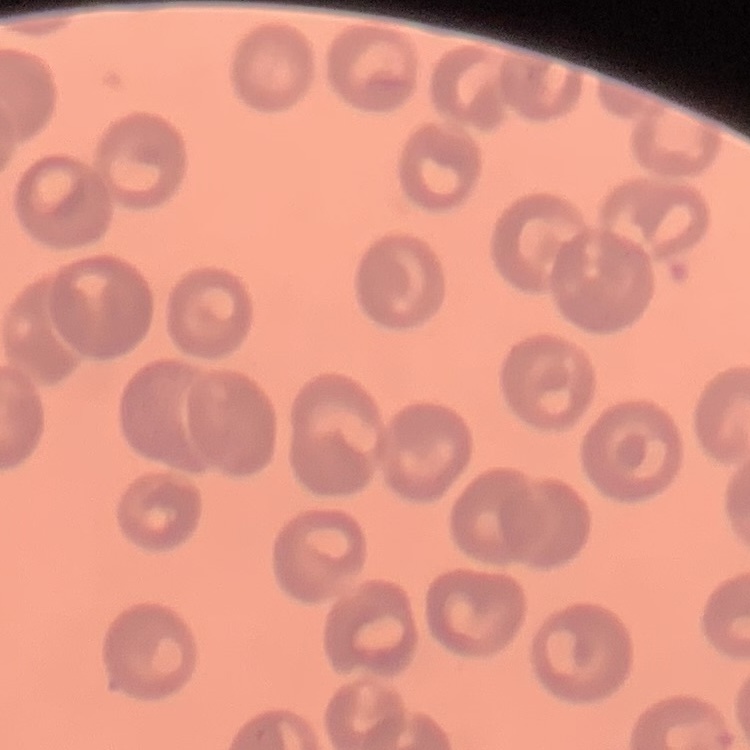

red blood cell morphology = no rouleaux formation
image type = square crop of a larger photomicrograph
preparation = thin blood smear
stain = Field's or Giemsa